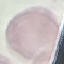

Summary:
  - Malaria status: uninfected
  - Capture: smartphone camera at the microscope eyepiece
  - Image type: automatically extracted cell patch, resized to 64 × 64 pixels
  - Preparation: thin smear
  - Stain: Giemsa